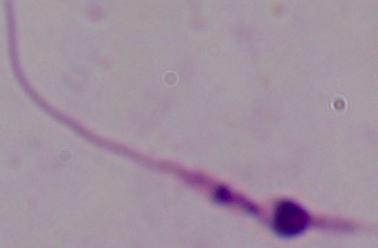

{
  "magnification": "1000x",
  "modality": "micrograph",
  "identification": "Leishmania"
}